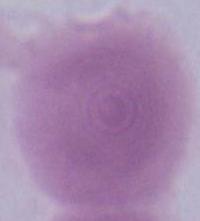

Summary:
  - Identification: red blood cell
  - Modality: micrograph
  - Magnification: 1000x